Locate and identify every blood parasite.
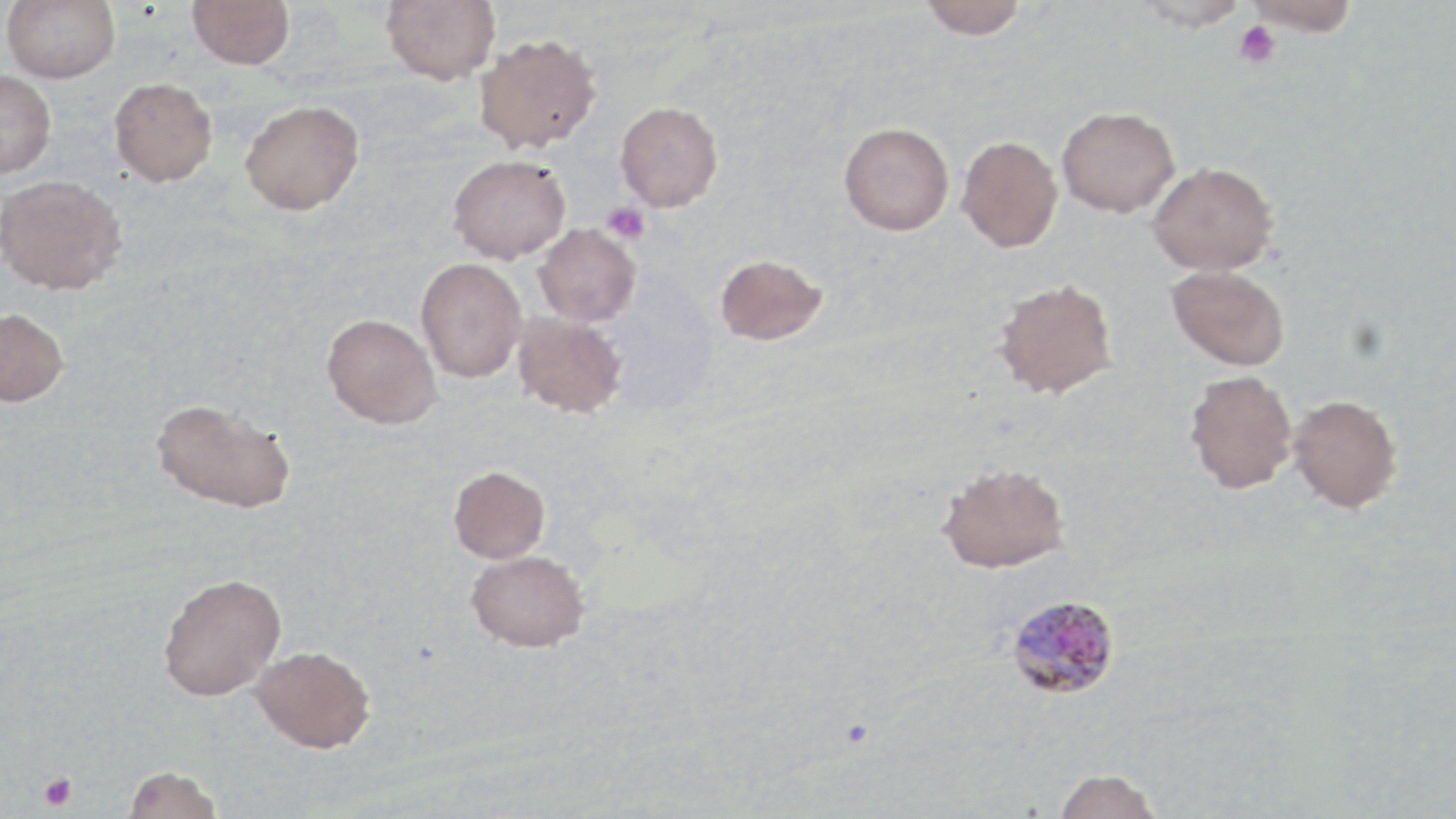

Approximate bounding boxes as named x1/y1/x2/y2 corners in pixels.
Plasmodium malariae-infected red blood cells: (x1=1005, y1=593, x2=1121, y2=701).
No Plasmodium falciparum, Plasmodium ovale, Plasmodium vivax, Babesia divergens, or Trypanosoma brucei observed.

slide-level diagnosis = Plasmodium malariae
stain = May-Grünwald-Giemsa
field of view = one of a larger specimen
magnification = 1000x
modality = light microscopy
preparation = thin blood smear
image size = 1456×819 pixels
uninfected red blood cell locations = approximate bounding boxes as named x1/y1/x2/y2 corners in pixels: (x1=2, y1=0, x2=120, y2=83), (x1=188, y1=0, x2=294, y2=70), (x1=380, y1=0, x2=500, y2=84), (x1=1243, y1=0, x2=1361, y2=36), (x1=919, y1=1, x2=1029, y2=39), (x1=1134, y1=1, x2=1251, y2=32), (x1=474, y1=33, x2=601, y2=153), (x1=0, y1=69, x2=57, y2=179), (x1=108, y1=77, x2=217, y2=187), (x1=240, y1=99, x2=364, y2=215), (x1=615, y1=101, x2=723, y2=212), (x1=1057, y1=105, x2=1180, y2=217), (x1=839, y1=122, x2=954, y2=235), (x1=956, y1=135, x2=1062, y2=252), (x1=447, y1=154, x2=571, y2=263), (x1=1148, y1=161, x2=1277, y2=275), (x1=0, y1=173, x2=126, y2=294), (x1=533, y1=224, x2=641, y2=326), (x1=715, y1=253, x2=828, y2=345), (x1=416, y1=258, x2=527, y2=383), (x1=1166, y1=265, x2=1289, y2=370), (x1=993, y1=277, x2=1118, y2=399), (x1=0, y1=307, x2=69, y2=407), (x1=322, y1=313, x2=442, y2=429), (x1=513, y1=313, x2=627, y2=418), (x1=1184, y1=370, x2=1298, y2=493), (x1=1287, y1=394, x2=1402, y2=513), (x1=151, y1=397, x2=295, y2=514), (x1=938, y1=462, x2=1070, y2=575), (x1=448, y1=466, x2=550, y2=564), (x1=466, y1=551, x2=589, y2=655), (x1=158, y1=573, x2=285, y2=703), (x1=250, y1=648, x2=376, y2=759), (x1=122, y1=769, x2=224, y2=819), (x1=1053, y1=769, x2=1161, y2=819)
platelet locations = approximate bounding boxes as named x1/y1/x2/y2 corners in pixels: (x1=1233, y1=21, x2=1281, y2=68), (x1=602, y1=202, x2=649, y2=244), (x1=38, y1=772, x2=79, y2=812)